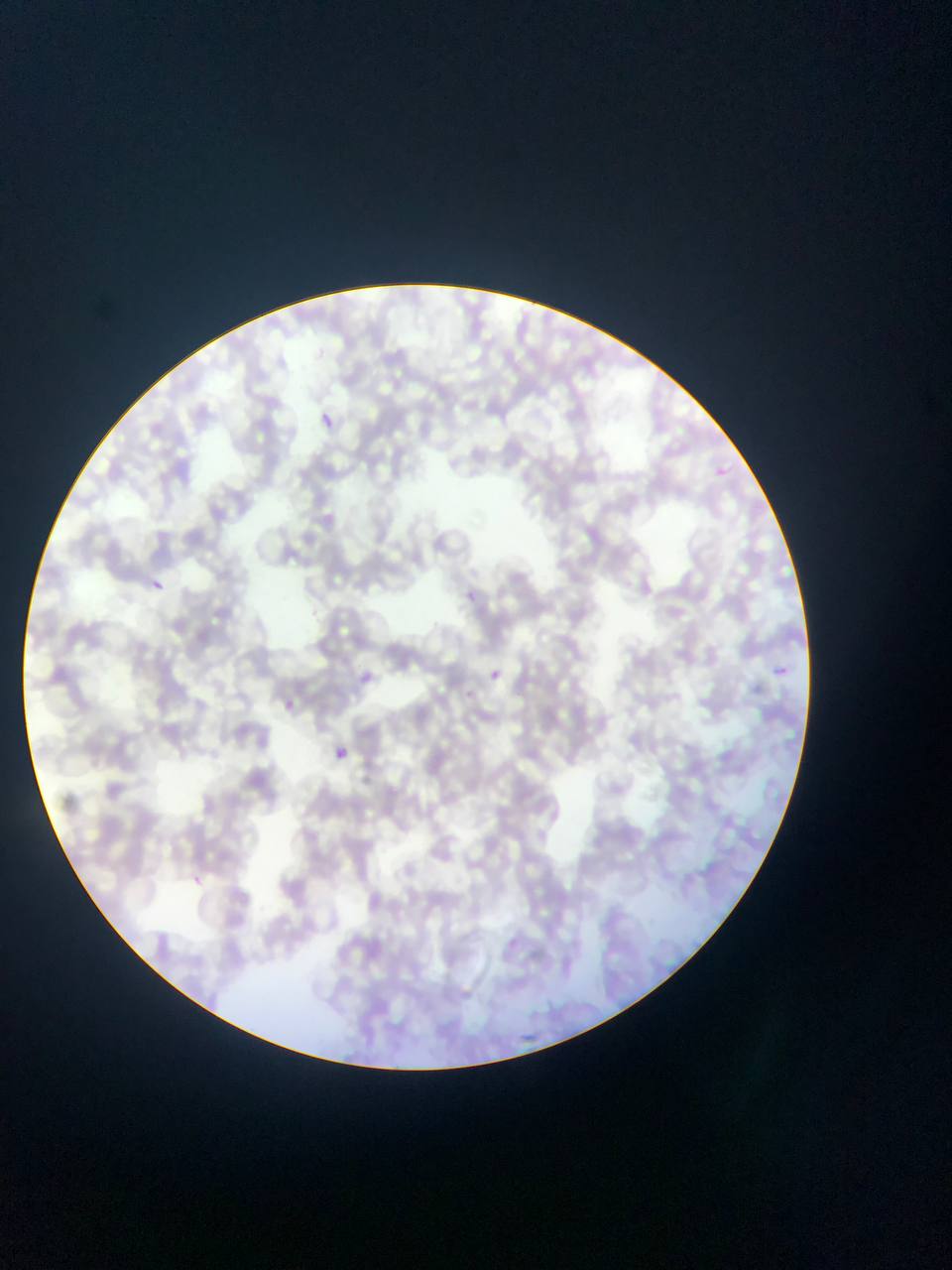 Approximate bounding boxes as {left, top, right, bottom} in pixels. Plasmodium parasite locations: {318, 409, 337, 428}, {719, 465, 736, 478}, {152, 580, 165, 591}, {465, 589, 483, 608}, {487, 666, 503, 683}, {772, 666, 791, 676}, {355, 670, 379, 691}, {280, 696, 310, 720}, {335, 746, 348, 759}, {188, 877, 204, 889}. Mobile-phone photograph taken through the microscope. Image is 952×1270 pixels. Thin blood film. Sample from Ghana. Single field of view.